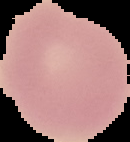
Summary:
  - Image size: 130×142 pixels
  - Preparation: thin blood smear
  - Image type: segmented cell region with the area outside set to black
  - Result: no malaria parasites seen